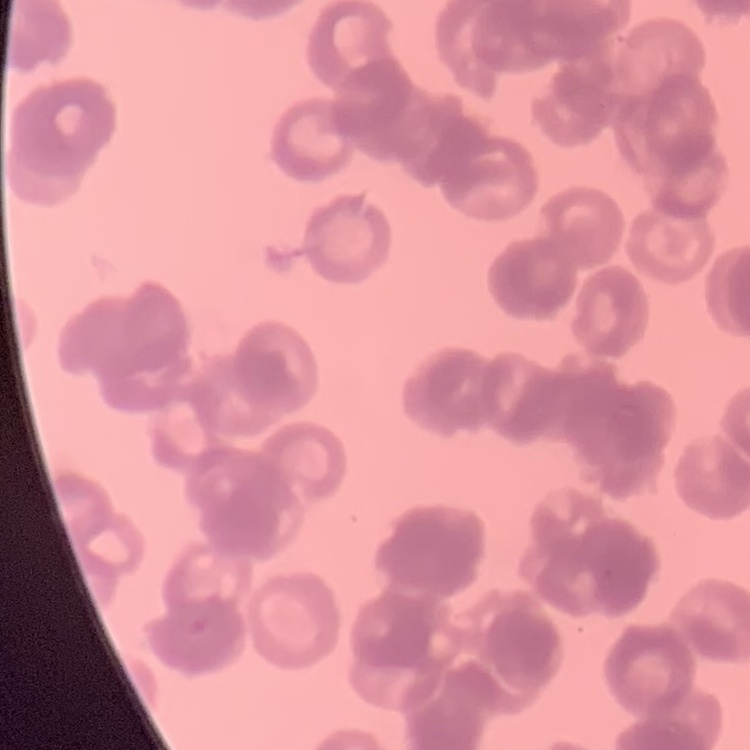
The red blood cells show rouleaux formation. Square crop of a larger photomicrograph. Stained with either Field's or Giemsa. Thin blood film.